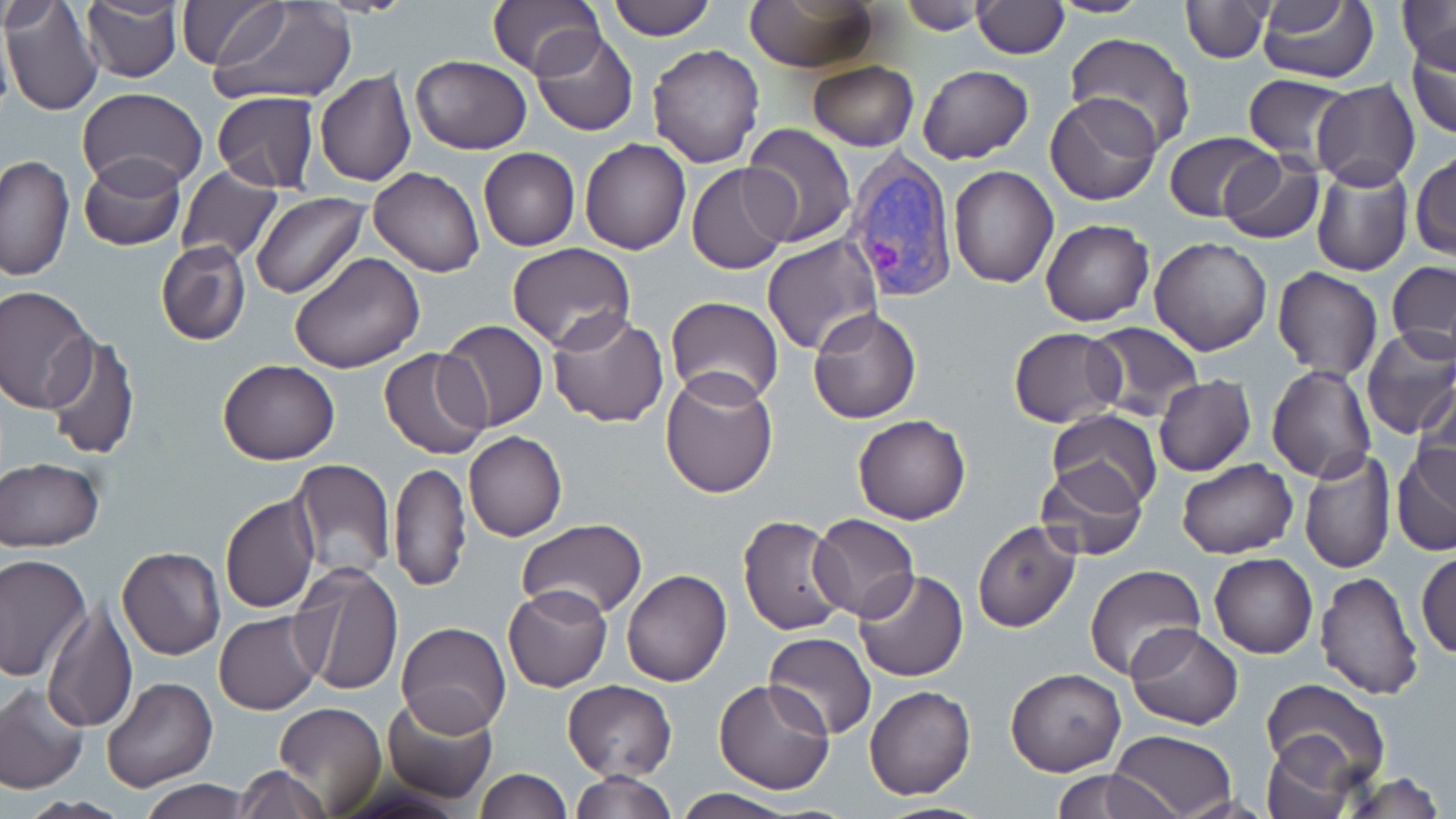
slide-level diagnosis = Plasmodium vivax
preparation = thin blood smear
uninfected red blood cell locations = approximate bounding boxes as (x1,y1)-(x2,y2) corner pairs in pixels: (80,0)-(182,84), (176,0)-(285,69), (605,0)-(716,40), (895,0)-(998,32), (1044,0)-(1154,18), (1179,0)-(1270,62), (0,1)-(104,115), (210,1)-(358,106), (489,1)-(602,79), (744,1)-(878,73), (972,1)-(1067,58), (1255,2)-(1379,84), (1397,2)-(1456,72), (3,4)-(64,36), (530,30)-(636,136), (1064,33)-(1196,154), (1406,33)-(1456,139), (648,45)-(764,169), (409,55)-(533,154), (808,60)-(918,150), (917,63)-(1033,164), (315,69)-(417,187), (1242,73)-(1353,164), (1312,79)-(1420,189), (78,87)-(206,191), (212,91)-(320,192), (1045,93)-(1162,205), (739,123)-(857,247), (1165,131)-(1277,221), (579,137)-(692,254), (478,147)-(580,251), (1411,150)-(1455,259), (1216,153)-(1325,245), (1,154)-(75,280), (78,156)-(186,252), (1309,159)-(1412,276), (686,162)-(795,274), (176,165)-(283,264), (949,166)-(1058,288), (369,168)-(485,277), (251,191)-(368,299), (1040,218)-(1154,326), (763,234)-(883,356), (1149,236)-(1273,355), (156,240)-(252,347), (506,243)-(636,351), (289,253)-(425,374), (1388,261)-(1456,358), (1271,267)-(1382,381), (0,287)-(96,412), (664,297)-(784,408), (809,308)-(922,423), (547,313)-(670,427), (437,320)-(548,431), (1083,323)-(1205,420), (1359,326)-(1456,440), (1008,327)-(1125,427), (40,333)-(140,460), (379,348)-(491,459), (217,359)-(341,464), (1266,364)-(1377,482), (660,368)-(780,498), (1153,374)-(1256,476), (1415,381)-(1456,493), (1045,410)-(1162,513), (853,414)-(971,524), (464,431)-(566,542), (1392,441)-(1456,558), (1297,445)-(1397,574), (0,457)-(103,551), (290,458)-(396,579), (1176,459)-(1298,559), (390,461)-(470,591), (1032,462)-(1149,565), (220,494)-(319,613), (808,512)-(919,622), (737,515)-(852,636), (516,519)-(647,620), (972,521)-(1081,633), (116,545)-(226,660), (1416,547)-(1455,661), (1208,553)-(1319,659), (0,554)-(90,681), (293,561)-(403,695), (1083,564)-(1206,681), (622,569)-(731,687), (852,569)-(969,682), (1314,570)-(1424,700), (502,584)-(611,692), (42,603)-(136,735), (214,612)-(322,714), (395,621)-(510,737), (1125,624)-(1243,730), (764,634)-(877,738), (1006,668)-(1126,776), (712,676)-(836,793), (102,677)-(218,792), (1261,679)-(1391,790), (562,680)-(677,780), (0,683)-(89,795), (865,685)-(975,800), (381,696)-(497,803), (274,701)-(387,816), (1110,729)-(1240,819), (1261,736)-(1357,819), (233,765)-(331,819), (1051,767)-(1178,818), (476,768)-(571,817), (570,771)-(678,818), (1342,773)-(1449,817), (140,780)-(252,819), (668,791)-(801,819), (17,796)-(130,818)
magnification = 1000x
field of view = single
modality = light microscopy
stain = May-Grünwald-Giemsa
image size = 1456×819 pixels
Plasmodium vivax-infected red blood cell locations = approximate bounding boxes as (x1,y1)-(x2,y2) corner pairs in pixels: (843,151)-(958,304)